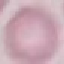 Result: negative for malaria parasites. Photographed with a smartphone camera at the microscope eyepiece. Giemsa stain. Automatically extracted cell patch, resized to 64 × 64 pixels. Thin smear of blood.